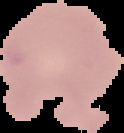
malaria_status: uninfected
image_size: 124×133 pixels
preparation: thin blood film
image_type: cell region segmented out of the field of view; surrounding area masked to black